Report the malaria status of this cell.
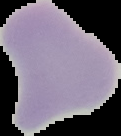
Uninfected.

{
  "image_size": "121×136 pixels",
  "preparation": "thin blood film",
  "image_type": "segmented cell region on a black background"
}